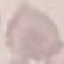 Malaria status: uninfected. Acquired by smartphone through the microscope eyepiece. Cell patch, automatically extracted from a larger field of view and resized to 64 × 64 pixels. Giemsa stain. Thin blood film.